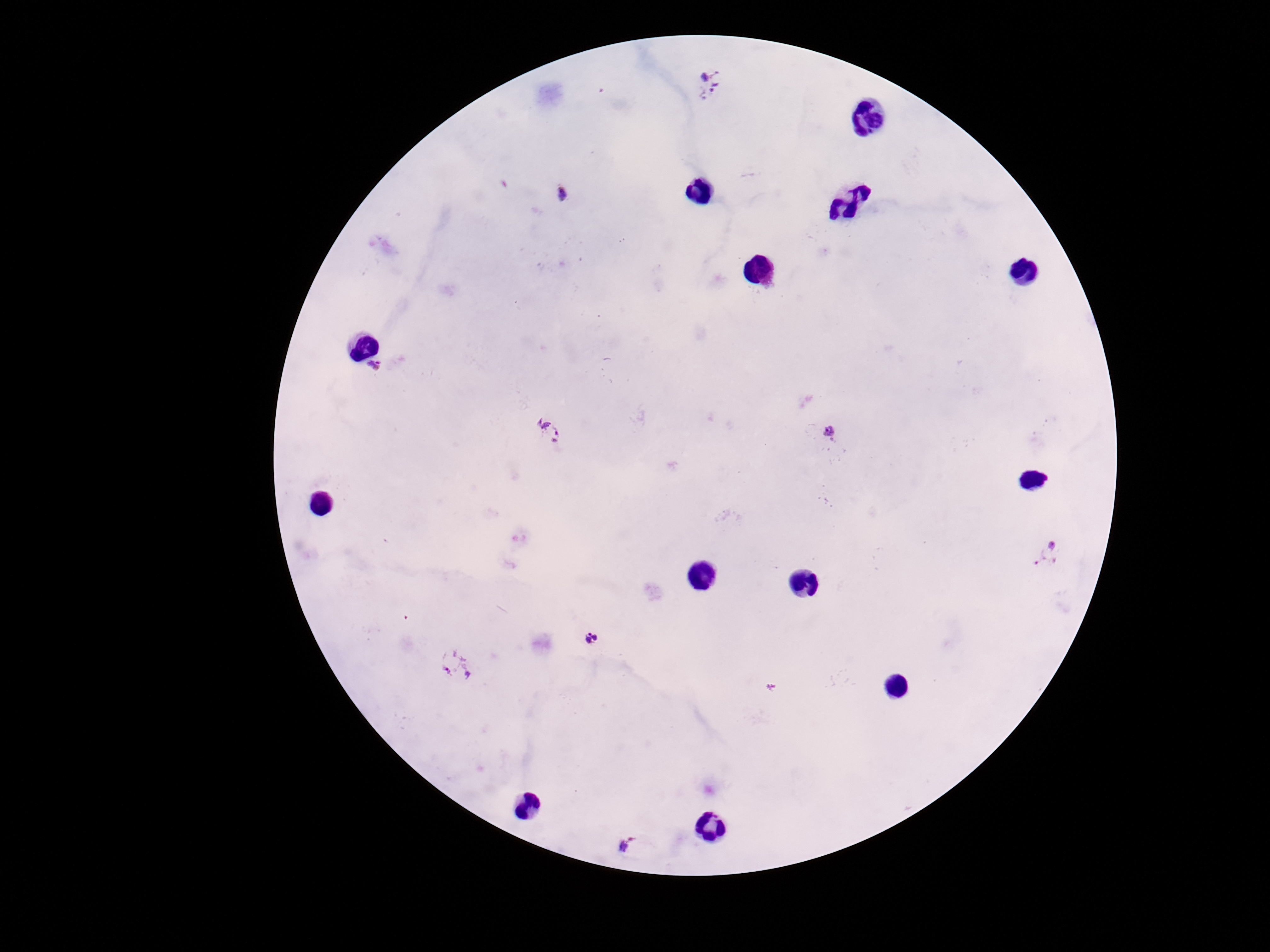

Approximate centers as {x, y} in pixels.
Summary:
  - Plasmodium parasite locations: {711, 82}, {562, 195}, {374, 366}, {828, 432}, {551, 433}, {1050, 554}, {590, 639}, {455, 664}, {627, 847}
  - Field of view: one from this slide
  - Patient malaria status: infected
  - Magnification: 100x
  - Capture: smartphone camera through the microscope eyepiece
  - Stain: Giemsa
  - Image size: 1270×952 pixels
  - Preparation: thick blood smear